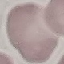

Summary:
  - Malaria status: uninfected
  - Preparation: thin blood film
  - Capture: smartphone camera at the microscope eyepiece
  - Image type: cell patch, automatically extracted from a larger field of view and resized to 64 × 64 pixels
  - Stain: Giemsa